State which parasite is depicted.
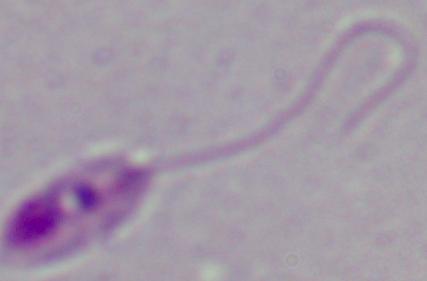
Leishmania.

Summary:
  - Magnification: 1000x
  - Modality: micrograph